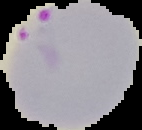
Summary:
  - Result: malaria parasites detected
  - Image size: 142×130 pixels
  - Image type: segmented cell region on a black background
  - Preparation: thin blood film